Report the malaria status of this cell.
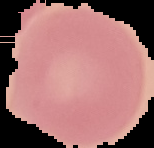

It is uninfected.

Image is 154×148 pixels. The area outside the segmented cell region is set to black. From a thin blood film.